Assess this cell for malaria.
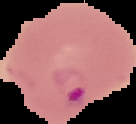
Parasitized.

Summary:
  - Image type: cell region segmented out of the field of view; surrounding area masked to black
  - Image size: 136×124 pixels
  - Preparation: thin blood smear